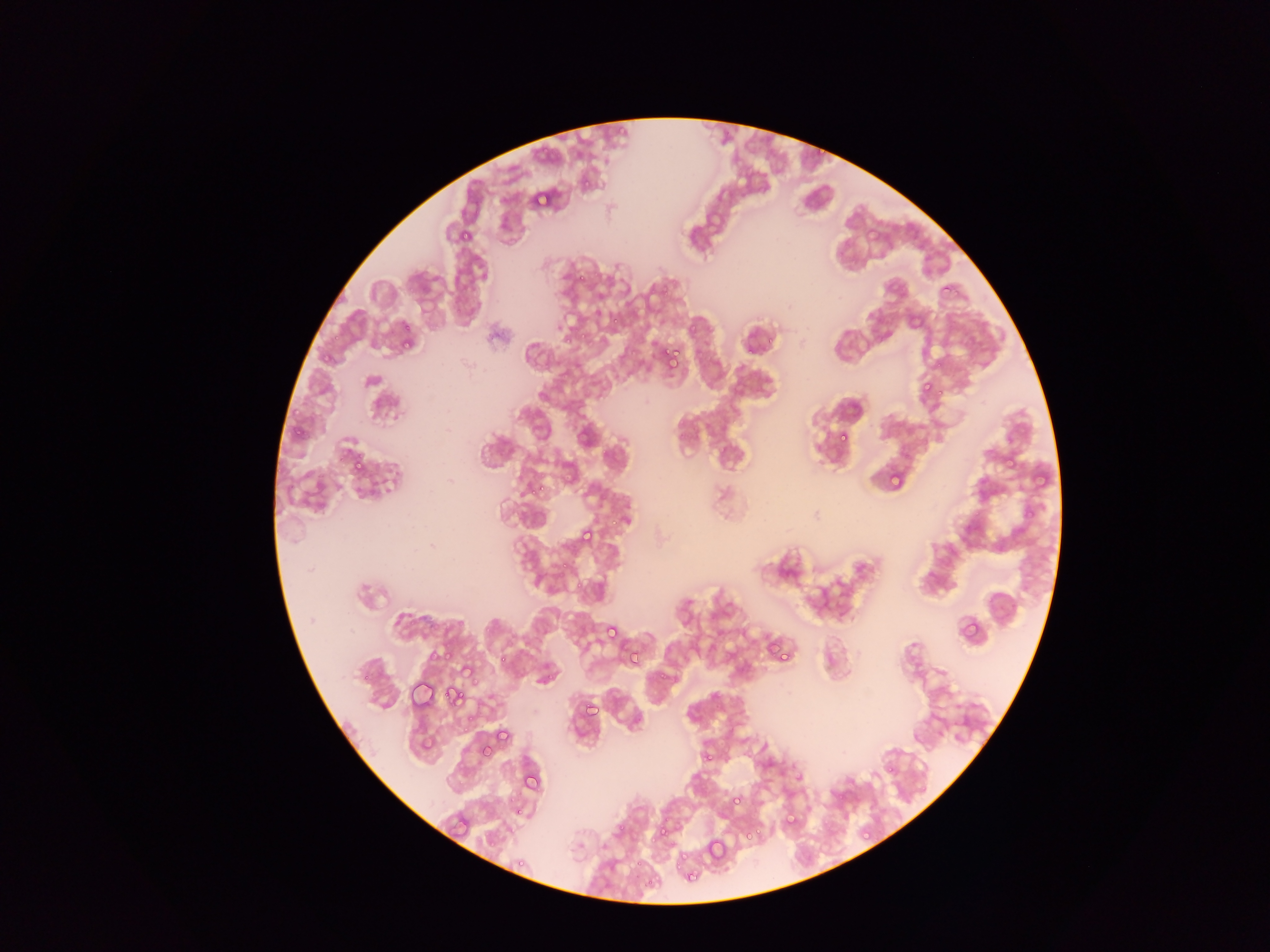
malaria parasite locations = approximate bounding boxes as [left, top, right, bottom] in pixels: [813, 138, 837, 159], [581, 172, 603, 189], [528, 187, 553, 211], [457, 224, 477, 242], [575, 255, 604, 284], [939, 280, 956, 298], [687, 320, 704, 339], [395, 324, 420, 351], [398, 336, 416, 354], [659, 345, 681, 367], [917, 378, 939, 402], [291, 404, 307, 417], [294, 422, 311, 444], [574, 423, 595, 450], [839, 431, 859, 445], [1005, 452, 1022, 470], [347, 455, 369, 478], [887, 469, 908, 493], [1031, 469, 1051, 491], [531, 478, 549, 498], [609, 515, 625, 532], [577, 525, 598, 548], [557, 558, 572, 570], [570, 576, 589, 593], [957, 616, 982, 642], [602, 622, 621, 642], [493, 643, 517, 669], [624, 645, 645, 669], [777, 649, 798, 663], [497, 651, 513, 669], [459, 662, 478, 683], [408, 682, 436, 713], [444, 684, 466, 708], [584, 700, 603, 719], [461, 708, 478, 725], [497, 718, 520, 744], [476, 743, 492, 761], [699, 748, 716, 765], [884, 766, 898, 779], [520, 769, 544, 796], [732, 790, 752, 808], [514, 799, 528, 818], [451, 811, 472, 833], [778, 811, 799, 833], [653, 820, 673, 844], [740, 826, 757, 845], [860, 826, 876, 843], [485, 834, 501, 848], [702, 835, 729, 866], [513, 852, 533, 868], [680, 864, 702, 888]
capture = mobile-phone photograph through a microscope
image size = 1270×952 pixels
preparation = thin blood smear
country = Ghana
field of view = single